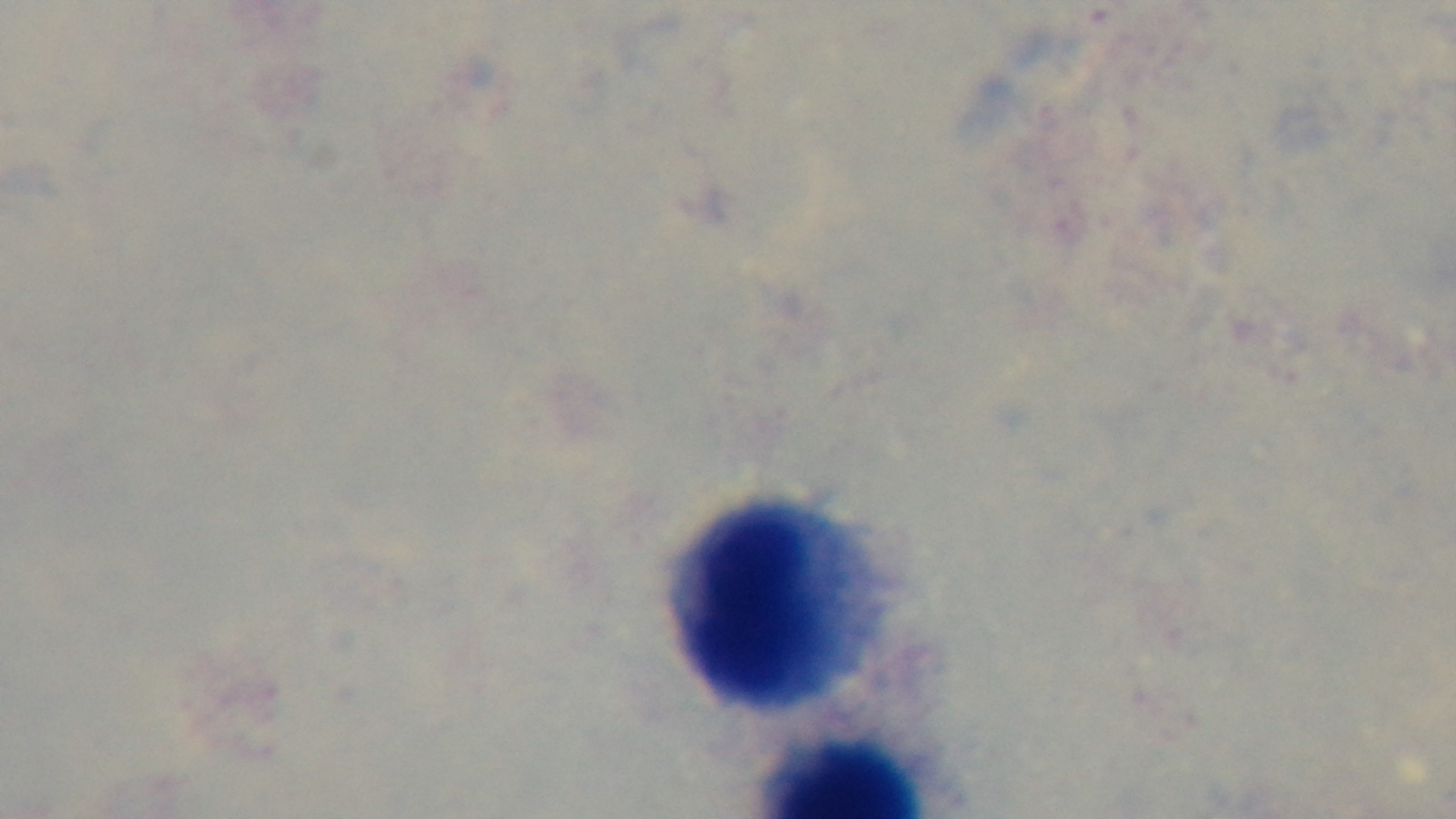

Preparation: thick. Light microscopy. 100x oil-immersion objective. Giemsa stain. Malaria status: uninfected. Single field of view. Captured with a mounted 4K digital camera.